Point out each leukocyte.
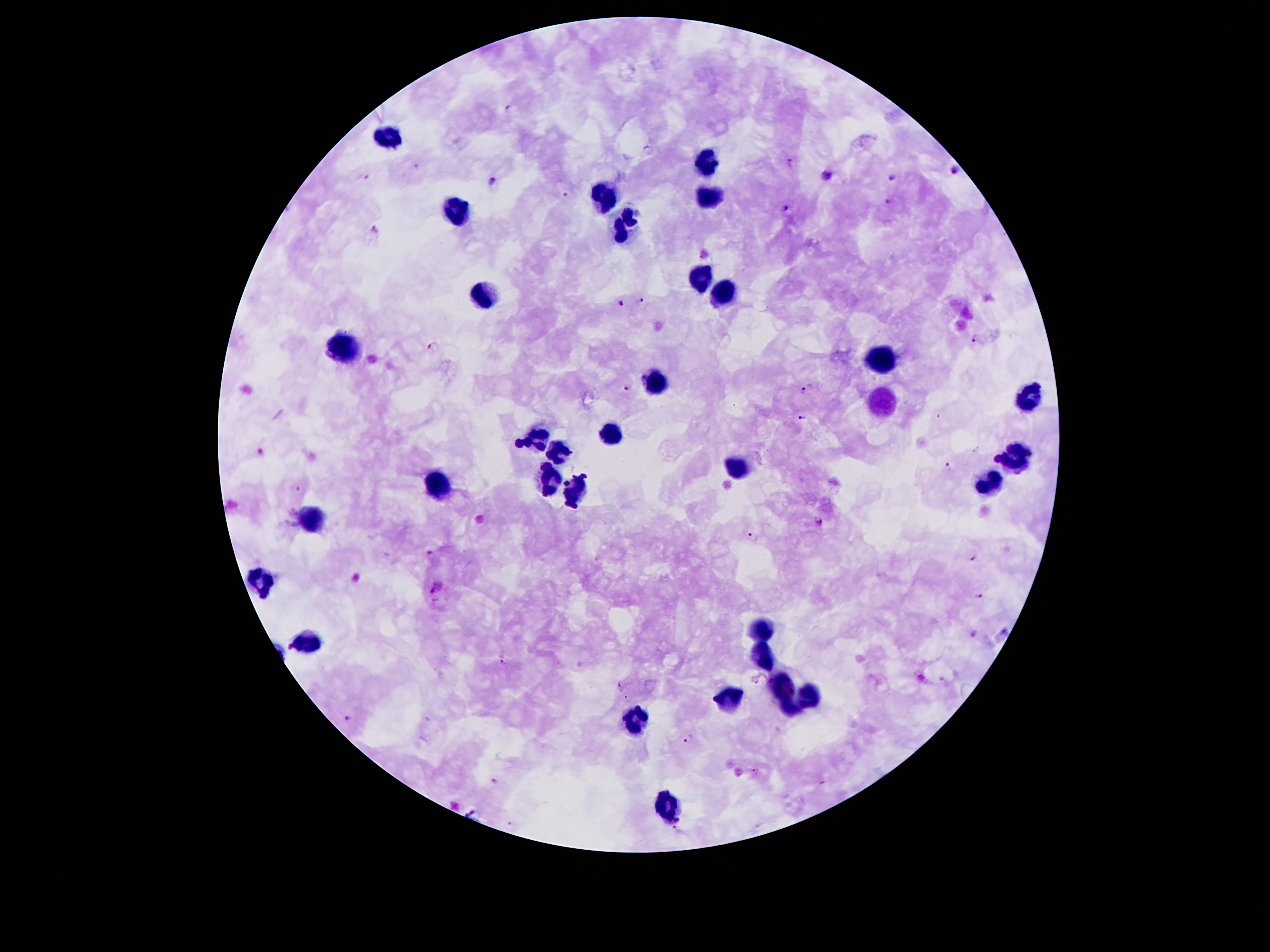

Approximate object centers, in pixels from the top-left corner.
Leukocytes: (x=391, y=134), (x=704, y=162), (x=709, y=196), (x=606, y=199), (x=456, y=208), (x=627, y=223), (x=701, y=280), (x=485, y=290), (x=722, y=294), (x=345, y=347), (x=881, y=357), (x=663, y=381), (x=1028, y=396), (x=881, y=402), (x=613, y=435), (x=536, y=436), (x=521, y=442), (x=557, y=451), (x=1017, y=457), (x=547, y=464), (x=736, y=465), (x=551, y=477), (x=990, y=484), (x=441, y=485), (x=583, y=486), (x=548, y=492), (x=572, y=498), (x=313, y=518), (x=261, y=583), (x=763, y=627), (x=306, y=640), (x=768, y=656), (x=780, y=690), (x=811, y=696), (x=728, y=697), (x=794, y=709), (x=631, y=720), (x=668, y=812).

malaria parasite locations = (x=508, y=108), (x=648, y=149), (x=791, y=161), (x=956, y=170), (x=828, y=175), (x=892, y=176), (x=361, y=177), (x=493, y=181), (x=565, y=194), (x=887, y=201), (x=785, y=208), (x=375, y=228), (x=643, y=299), (x=620, y=304), (x=972, y=338), (x=435, y=345), (x=629, y=388), (x=807, y=389), (x=803, y=416), (x=263, y=452), (x=996, y=460), (x=948, y=465), (x=586, y=475), (x=567, y=483), (x=298, y=488), (x=565, y=505), (x=575, y=507), (x=820, y=522), (x=753, y=535), (x=430, y=551), (x=971, y=556), (x=439, y=587), (x=979, y=595), (x=976, y=635), (x=502, y=659), (x=759, y=680), (x=620, y=687), (x=627, y=698), (x=349, y=717), (x=689, y=740), (x=754, y=771), (x=494, y=780)
image size = 1270×952 pixels
patient malaria status = positive for Plasmodium falciparum
capture = smartphone through the microscope eyepiece
magnification = 100x
field of view = single
preparation = thick blood film
stain = Giemsa